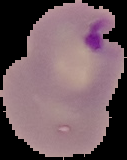
{
  "malaria_status": "parasitized",
  "image_size": "127×160 pixels",
  "image_type": "cell region segmented out of the field of view; surrounding area masked to black",
  "preparation": "thin blood film"
}